Assess this cell for malaria.
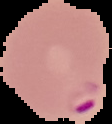
Parasitized.

From a thin blood smear. Image is 112×124 pixels. Segmented cell region on a black background.